Describe the morphology of the erythrocytes.
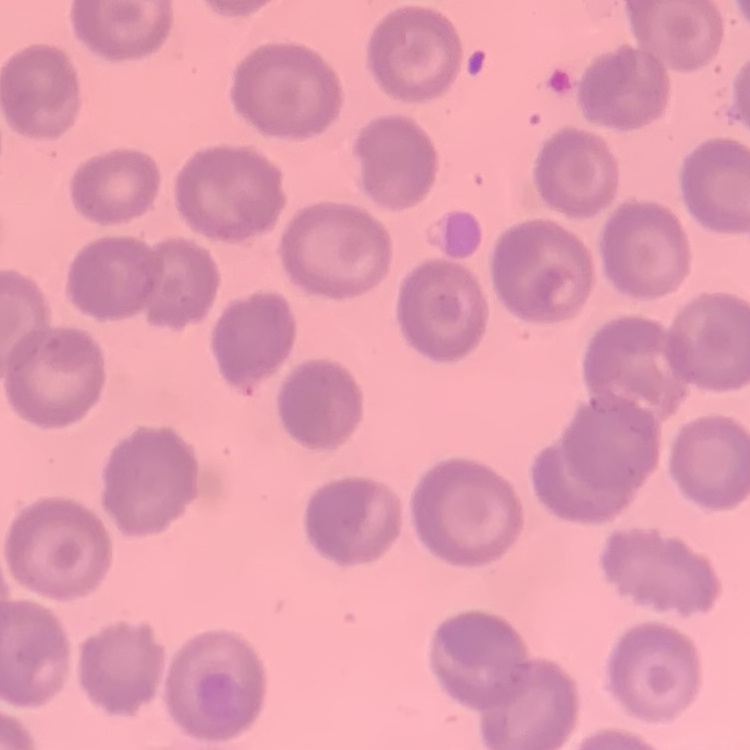

They show no rouleaux formation.

Square crop of a larger photomicrograph. Thin peripheral smear. Stained with either Field's or Giemsa.